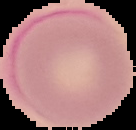

image type = segmented cell region with the area outside set to black
malaria status = uninfected
preparation = thin blood film
image size = 136×130 pixels